Describe the morphology of the red blood cells.
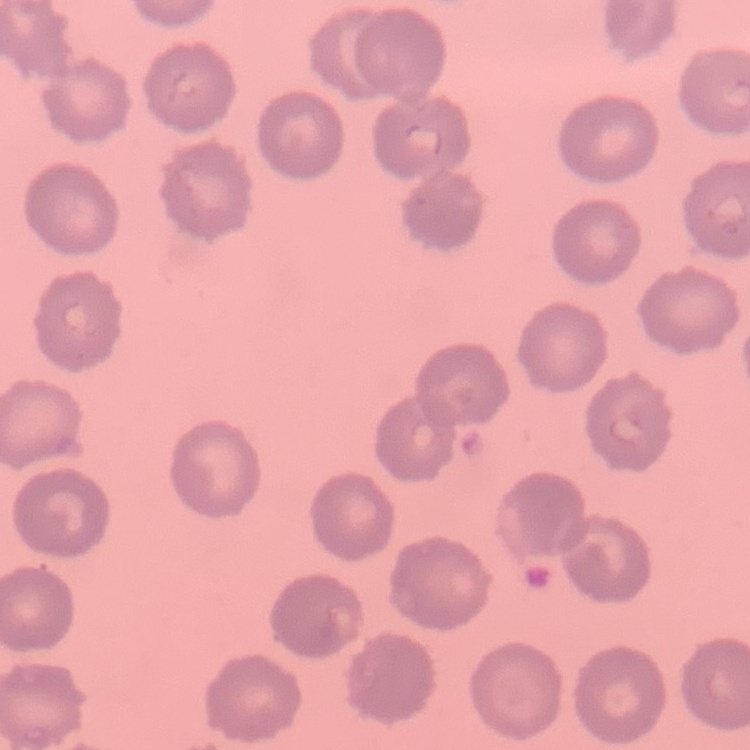

They show no rouleaux formation.

Summary:
  - Image type: one tile cut from a larger photomicrograph
  - Preparation: thin peripheral smear
  - Stain: Field's or Giemsa